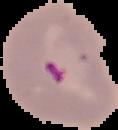

Cell region segmented out of the field of view; the surrounding area is masked to black. From a thin blood film. Result: malaria parasites detected. Image is 118×130 pixels.